Describe the morphology of the erythrocytes.
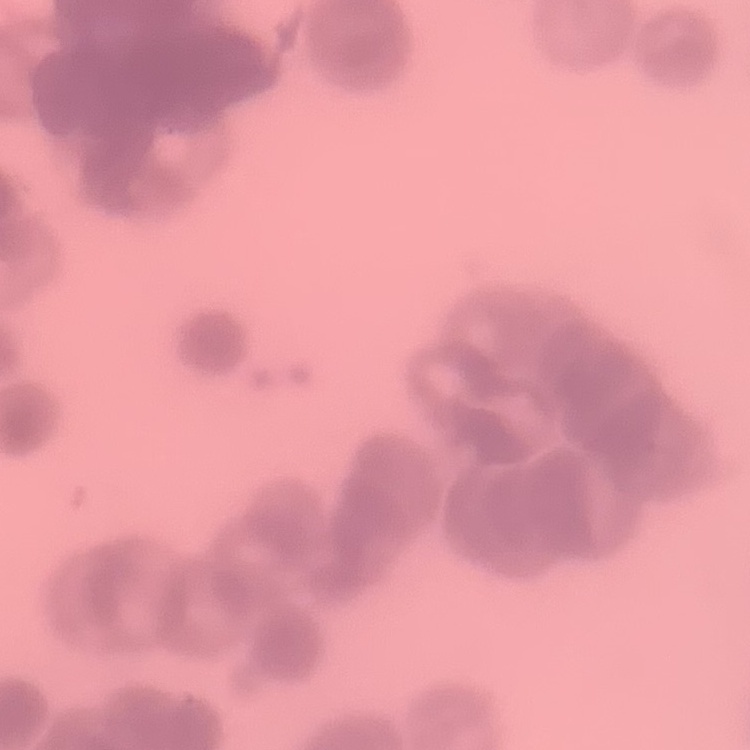

They show rouleaux formation.

Stained with either Field's or Giemsa. Thin peripheral smear. One tile cut from a larger photomicrograph.